State the preparation type.
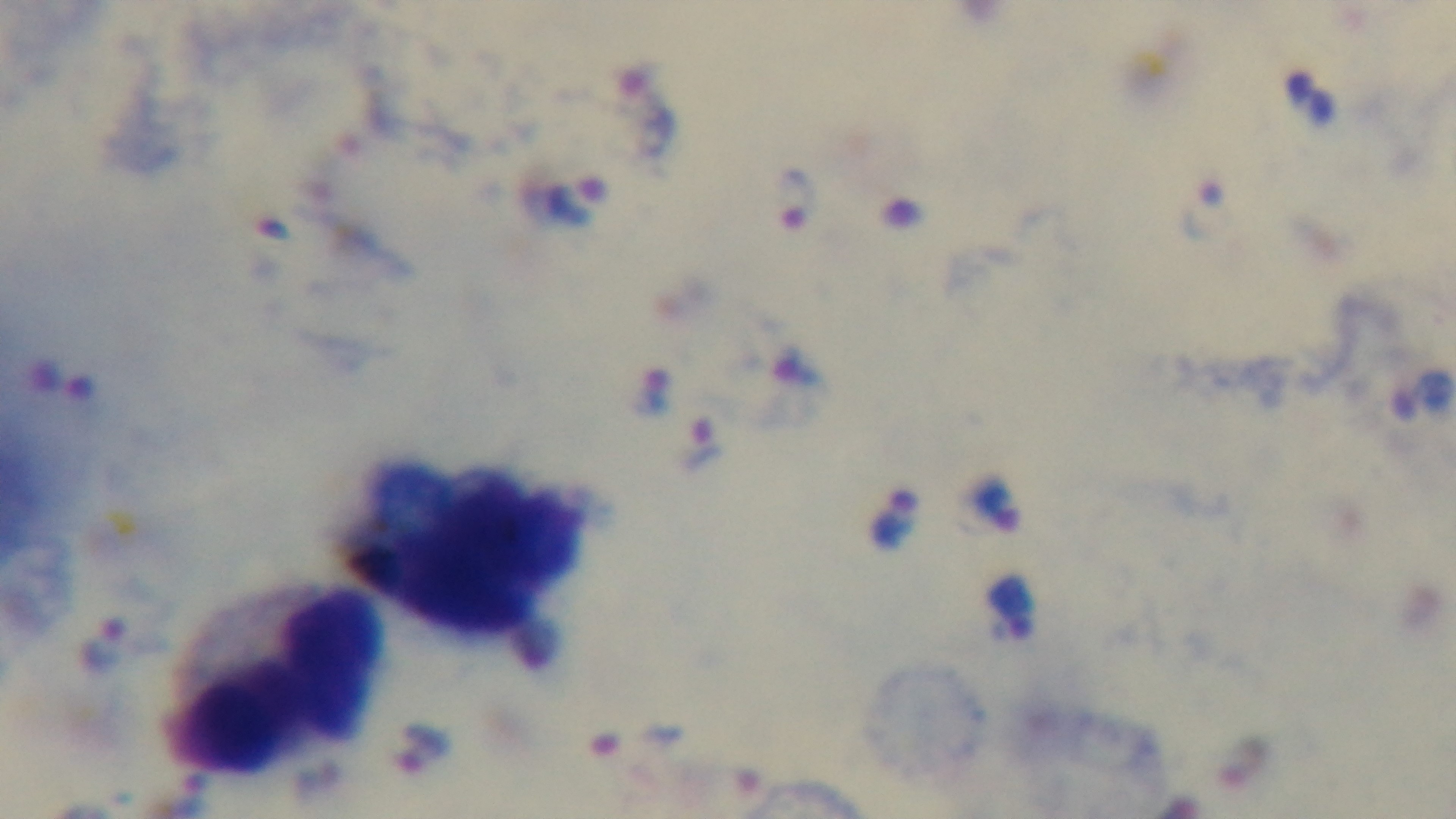

It is a thick blood film.

objective = 100x oil immersion
stain = Giemsa
capture = mounted 4K digital camera
modality = light microscopy
malaria status = infected
field of view = single